State which parasite is depicted.
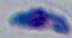

This is Toxoplasma gondii.

Summary:
  - Modality: photomicrograph
  - Magnification: 1000x